Outline each Plasmodium ovale-infected red blood cell.
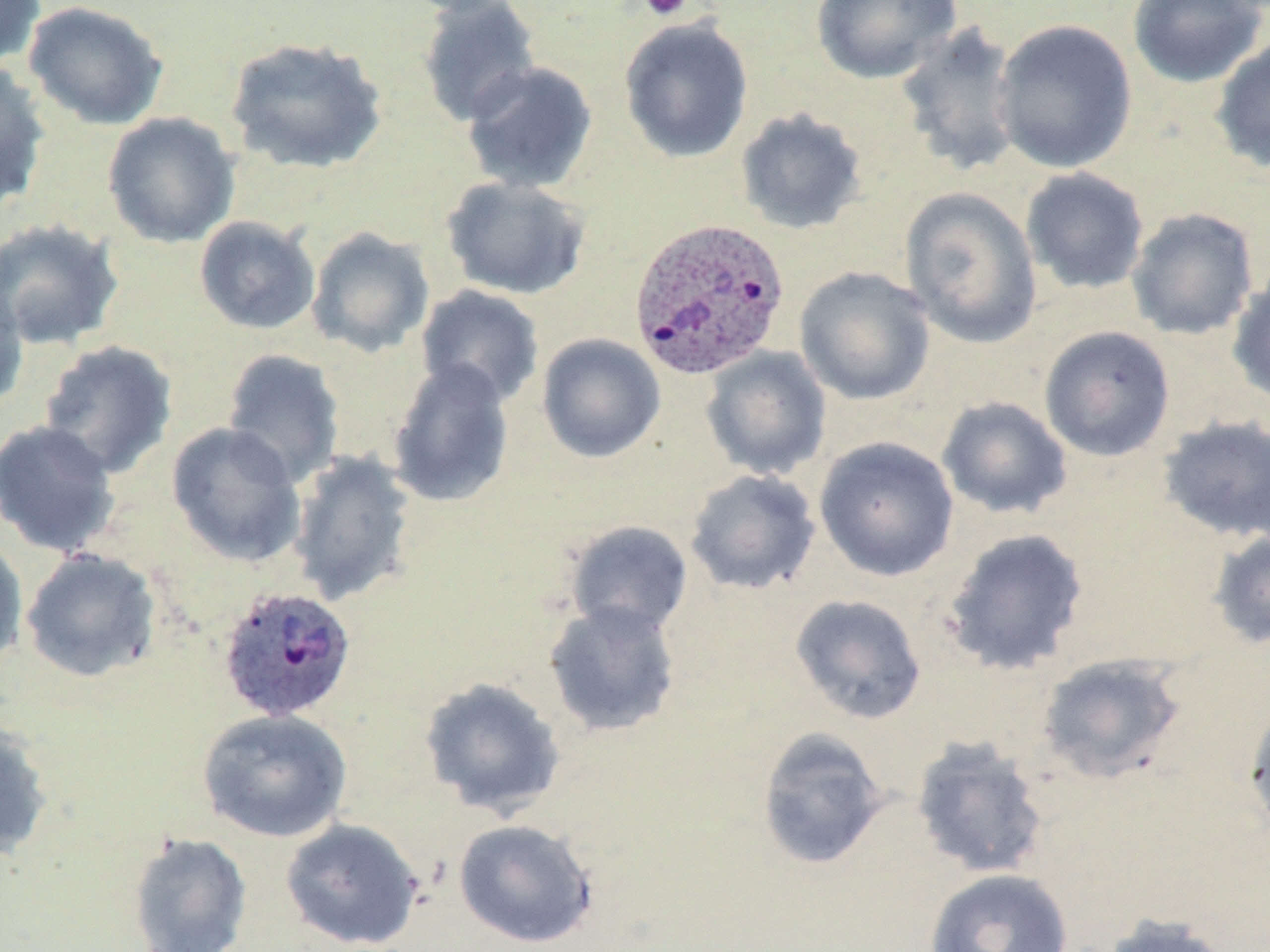

Approximate bounding boxes as [x1, y1, x2, y2] in pixels.
Plasmodium ovale-infected red blood cells: [628, 216, 790, 381], [216, 585, 357, 724].

{
  "slide_level_diagnosis": "Plasmodium ovale",
  "magnification": "1000x",
  "stain": "May-Grünwald-Giemsa",
  "image_size": "1270×952 pixels",
  "modality": "light microscopy",
  "field_of_view": "single",
  "platelet_locations": "approximate bounding boxes as [x1, y1, x2, y2] in pixels: [639, 0, 692, 21]",
  "uninfected_red_blood_cell_locations": "approximate bounding boxes as [x1, y1, x2, y2] in pixels: [0, 0, 46, 68], [395, 0, 527, 18], [811, 0, 961, 85], [1127, 0, 1267, 88], [22, 1, 169, 131], [417, 1, 541, 127], [619, 17, 754, 163], [992, 18, 1138, 174], [894, 22, 1027, 177], [224, 36, 388, 174], [1211, 36, 1270, 174], [0, 60, 52, 210], [461, 61, 599, 194], [735, 108, 868, 235], [102, 112, 241, 249], [1020, 167, 1149, 295], [440, 176, 592, 300], [899, 187, 1043, 348], [1126, 207, 1259, 341], [194, 215, 321, 335], [0, 218, 124, 350], [306, 226, 435, 358], [1227, 265, 1270, 407], [794, 267, 935, 405], [0, 272, 29, 415], [415, 285, 545, 408], [1038, 326, 1175, 461], [536, 333, 666, 463], [38, 340, 178, 478], [701, 346, 831, 480], [221, 348, 345, 488], [387, 359, 515, 509], [937, 396, 1072, 520], [1157, 415, 1270, 543], [0, 419, 121, 558], [166, 422, 307, 568], [814, 436, 959, 583], [287, 450, 419, 607], [684, 468, 821, 595], [563, 520, 693, 637], [941, 528, 1089, 675], [1207, 528, 1270, 651], [0, 534, 29, 671], [20, 548, 162, 683], [789, 593, 927, 725], [543, 600, 682, 738], [1038, 653, 1186, 784], [419, 677, 567, 819], [1243, 698, 1270, 838], [197, 708, 352, 843], [0, 716, 54, 862], [756, 726, 890, 871], [910, 735, 1051, 879], [280, 818, 425, 950], [452, 818, 598, 948], [127, 832, 253, 952], [924, 867, 1073, 952], [1101, 914, 1234, 952]",
  "preparation": "thin blood film"
}